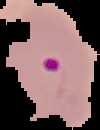
Summary:
  - Result: Plasmodium parasites detected
  - Preparation: thin blood film
  - Image type: segmented cell region on a black background
  - Image size: 100×130 pixels